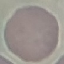

malaria status = uninfected
capture = smartphone through the microscope eyepiece
image type = cell patch, automatically extracted from a larger field of view and resized to 64 × 64 pixels
preparation = thin blood smear
stain = Giemsa